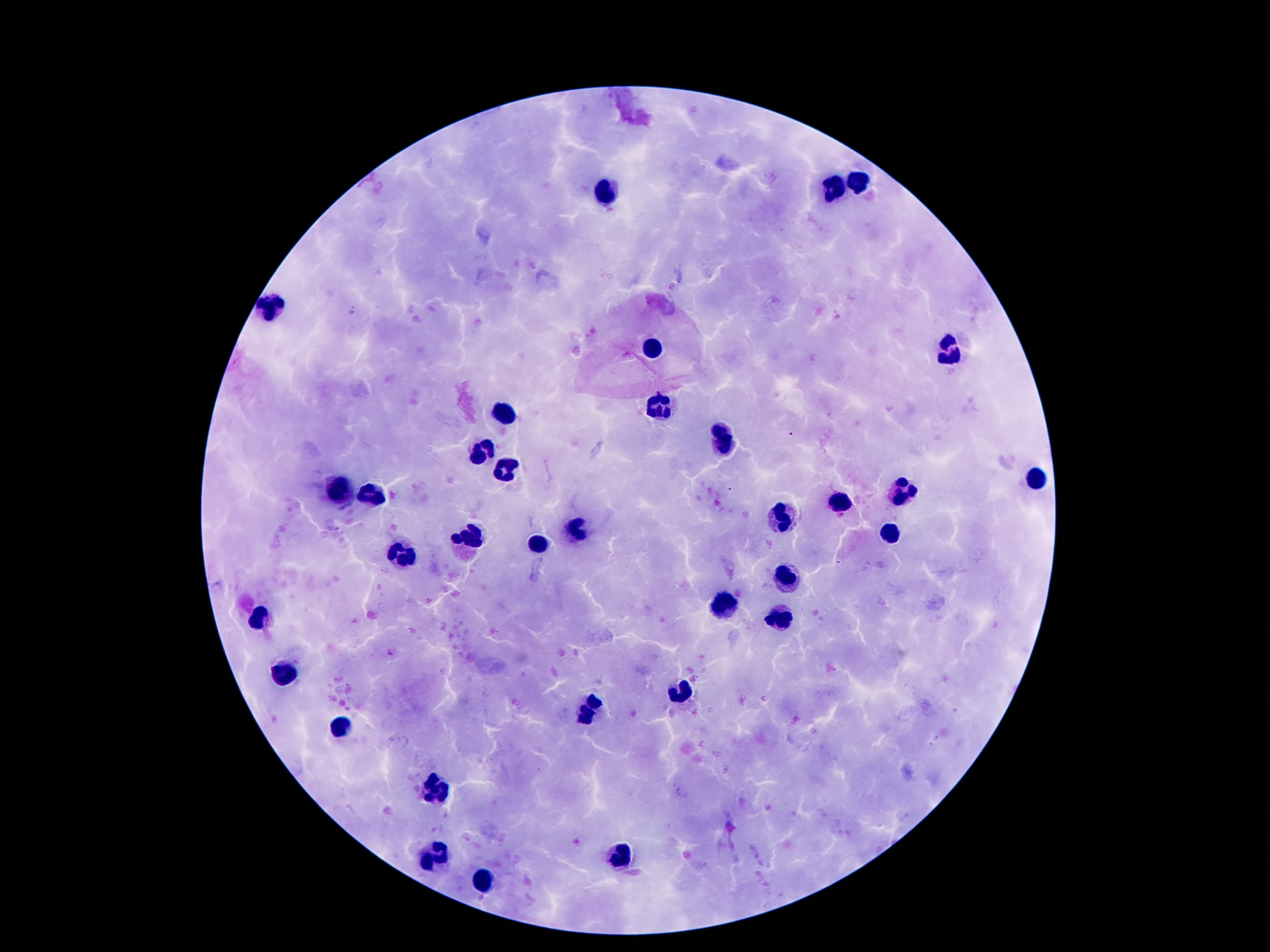
patient malaria status = not infected
magnification = 100x
capture = smartphone camera through the microscope eyepiece
leukocyte locations = approximate centers as [x, y] in pixels: [862, 182], [838, 189], [606, 193], [272, 302], [653, 345], [950, 351], [660, 403], [502, 411], [721, 443], [487, 450], [510, 465], [1038, 478], [375, 489], [338, 493], [907, 493], [840, 504], [785, 515], [578, 526], [891, 534], [469, 536], [539, 544], [402, 553], [787, 577], [723, 607], [262, 615], [782, 620], [285, 671], [682, 689], [590, 709], [342, 725], [438, 791], [619, 857], [436, 859], [487, 879]
preparation = thick peripheral-blood smear
stain = Giemsa
image size = 1270×952 pixels
field of view = single